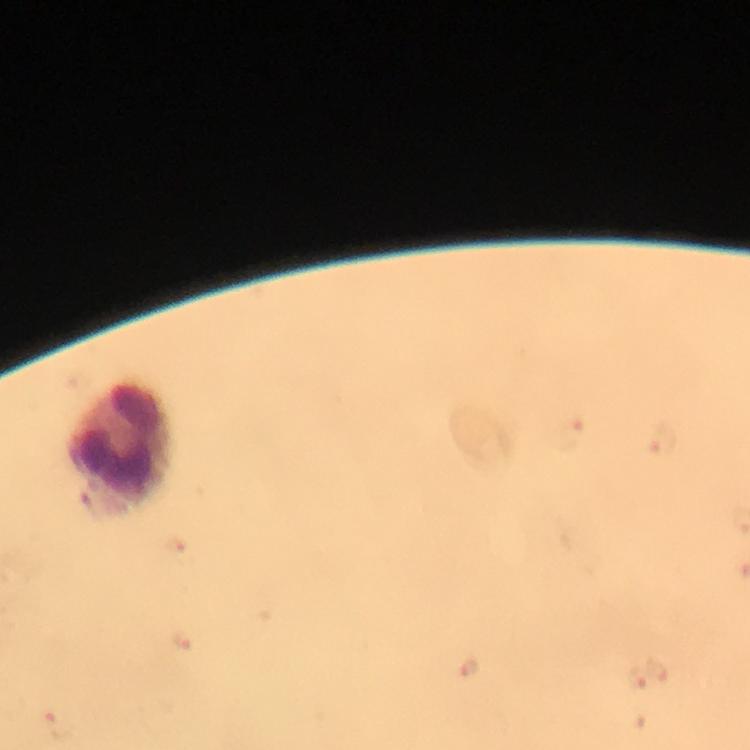
Approximate centers as (x, y) in pixels. Leukocyte locations: (121, 449). At 100x magnification. Image is 750×750 pixels. Cropped region of a single field of view. Malaria parasites: none detected. Immersion oil applied. From a malaria diagnostic workup. Thick smear. Giemsa stain. Smartphone photograph taken through a microscope.